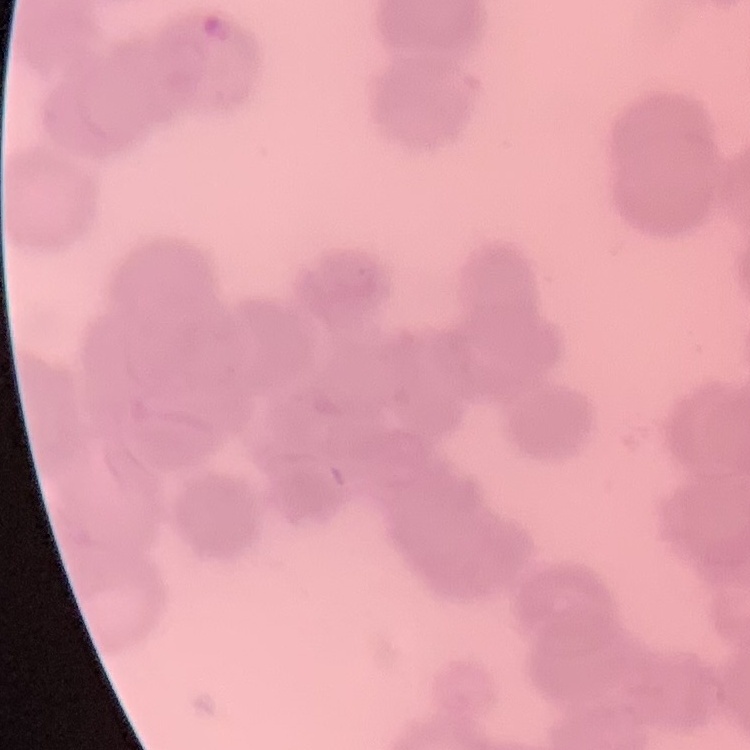

erythrocyte morphology = rouleaux formation
preparation = thin blood film
stain = Field's or Giemsa
image type = one tile cut from a larger photomicrograph